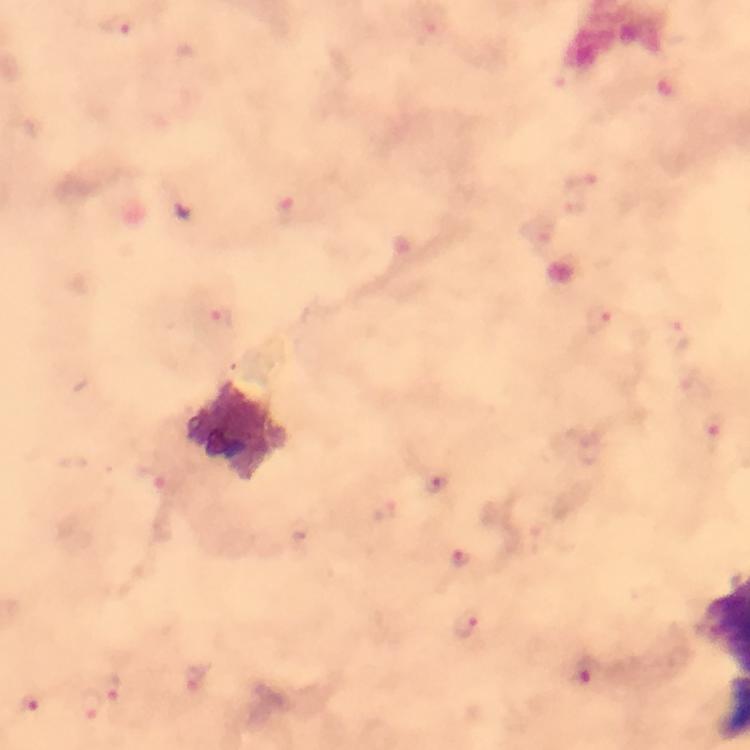 Approximate centers as [x, y] in pixels. Malaria parasite locations: [604, 318], [715, 426], [437, 485], [464, 559], [466, 622], [590, 672], [113, 688], [30, 701], [93, 704]. Image is 750×750 pixels. Cropped region of a single field of view. Smartphone photograph taken through a microscope. 100x magnification. Giemsa-stained preparation. From a diagnostic examination for malaria. Thick smear. Immersion oil was used.